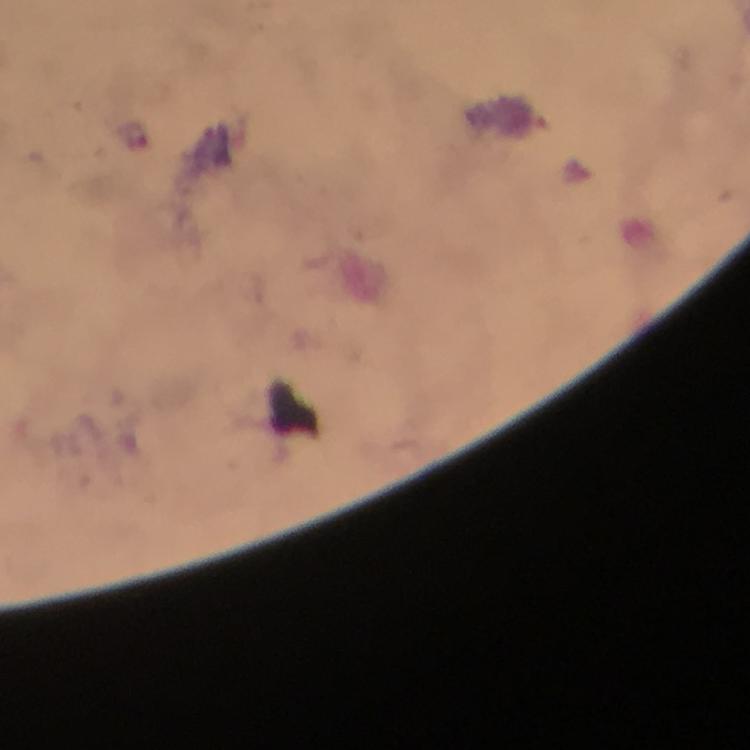

Approximate object centers, in pixels from the top-left corner. Plasmodium parasite locations: (x=133, y=133). Giemsa stain. Photographed through the microscope with a smartphone camera. At 100x magnification. Thick blood smear. Immersion oil applied. From a diagnostic examination for malaria. A crop from one field of view. Image is 750×750 pixels.